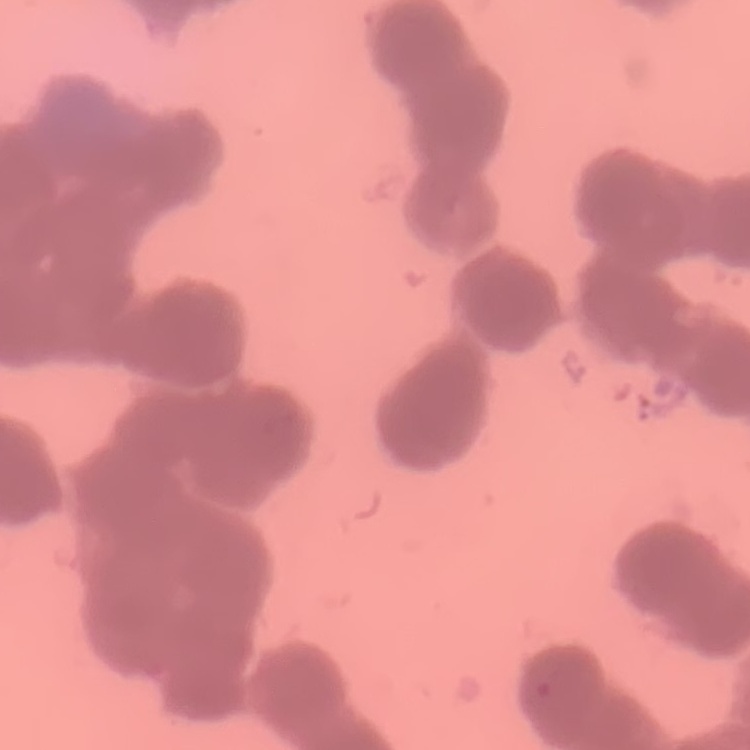

Summary:
  - Red blood cell morphology: rouleaux formation
  - Preparation: thin peripheral smear
  - Image type: one tile cut from a larger photomicrograph
  - Stain: Field's or Giemsa